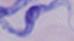 1000x magnification. Photomicrograph. A trypanosome is shown.